Report the malaria status of this cell.
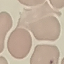

It is uninfected.

Summary:
  - Capture: smartphone camera at the microscope eyepiece
  - Preparation: thin smear
  - Image type: automatically extracted cell patch, resized to 64 × 64 pixels
  - Stain: Giemsa